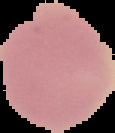

result = no Plasmodium parasites seen
image type = segmented cell region with the area outside set to black
preparation = thin blood film
image size = 115×133 pixels